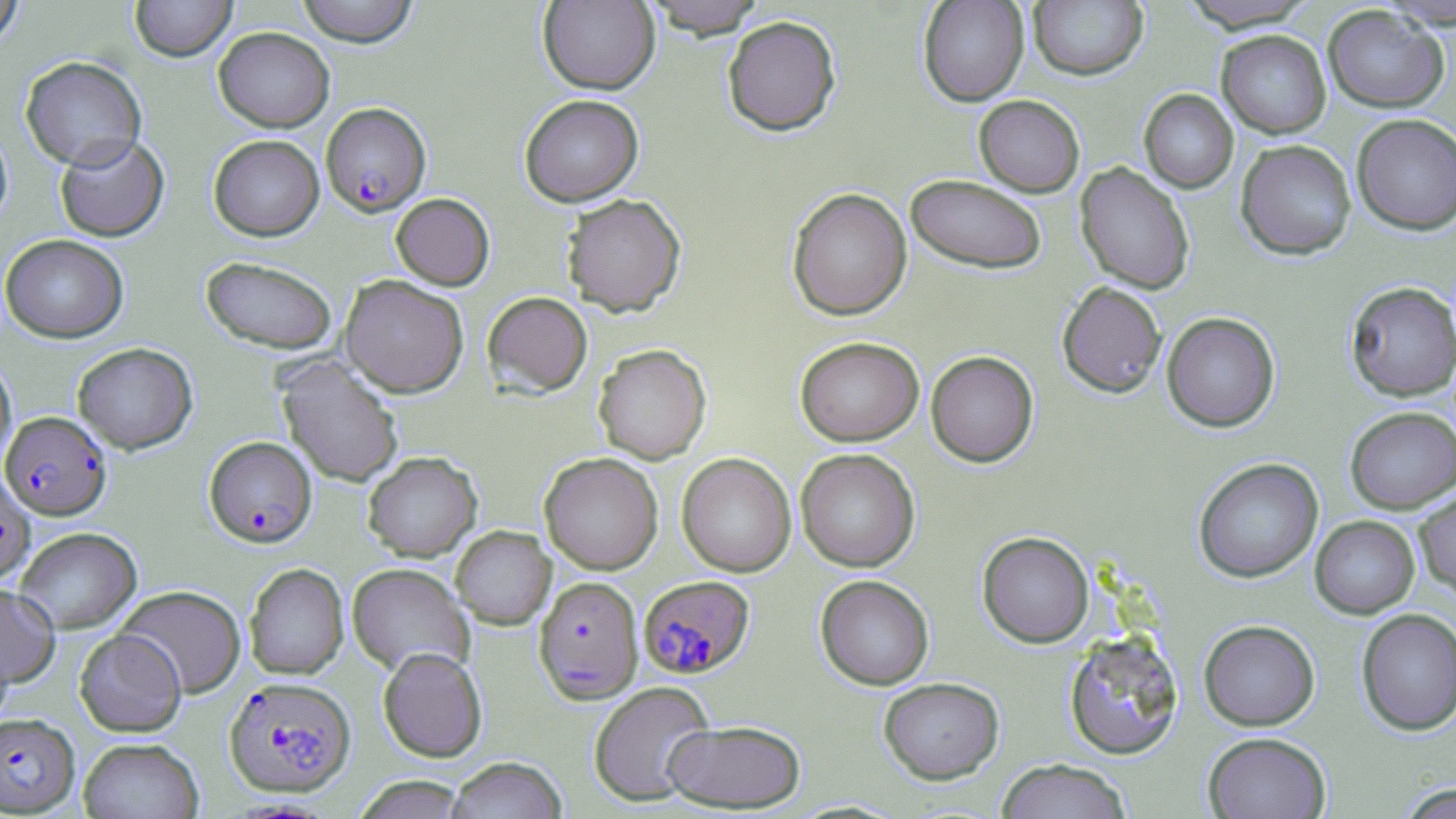

plasmodium_falciparum_infected_red_blood_cell_locations: 'approximate bounding boxes as (x1,y1)-(x2,y2) corner pairs in pixels: (321,102)-(431,216), (0,411)-(112,520), (204,436)-(317,546), (0,471)-(36,583), (639,575)-(754,677), (534,576)-(643,703), (225,676)-(355,796), (0,713)-(79,815)'
slide_level_diagnosis: Plasmodium falciparum
preparation: thin blood film
field_of_view: single
image_size: 1456×819 pixels
stain: May-Grünwald-Giemsa
magnification: 1000x
modality: light microscopy
uninfected_red_blood_cell_locations: 'approximate bounding boxes as (x1,y1)-(x2,y2) corner pairs in pixels: (130,0)-(237,61), (296,0)-(420,46), (642,0)-(767,37), (918,0)-(1029,106), (1375,0)-(1456,29), (0,1)-(25,49), (538,1)-(659,94), (1028,1)-(1148,80), (1179,1)-(1317,32), (1323,5)-(1449,113), (722,15)-(841,135), (214,27)-(335,132), (1216,30)-(1331,138), (20,56)-(147,170), (1139,89)-(1238,194), (519,94)-(644,206), (973,95)-(1085,197), (1352,115)-(1456,235), (0,123)-(13,230), (55,134)-(169,242), (209,134)-(324,240), (1235,139)-(1357,260), (1075,163)-(1195,294), (906,174)-(1048,274), (786,187)-(912,320), (391,192)-(494,290), (562,193)-(686,316), (0,234)-(129,342), (201,256)-(337,354), (341,275)-(469,397), (1057,281)-(1167,398), (1345,281)-(1456,402), (482,291)-(592,397), (1161,312)-(1280,432), (795,336)-(924,446), (73,342)-(198,454), (593,344)-(711,463), (925,350)-(1039,467), (0,355)-(16,471), (278,357)-(404,488), (1345,406)-(1456,513), (796,448)-(920,571), (362,451)-(482,562), (539,452)-(663,574), (677,452)-(796,577), (1193,457)-(1323,583), (1414,486)-(1456,600), (1310,515)-(1419,618), (451,525)-(556,629), (15,527)-(141,633), (977,531)-(1094,648), (244,563)-(349,679), (347,564)-(474,677), (815,574)-(934,690), (0,582)-(60,687), (116,585)-(246,697), (1356,608)-(1456,736), (1199,620)-(1320,730), (75,628)-(186,736), (1063,631)-(1184,760), (378,647)-(487,762), (878,677)-(1005,784), (588,681)-(715,806), (662,719)-(807,812), (1203,732)-(1331,819), (78,737)-(204,819), (445,756)-(567,819), (996,759)-(1133,819), (352,775)-(472,818), (1394,782)-(1456,819)'